Locate every Plasmodium vivax-infected red blood cell.
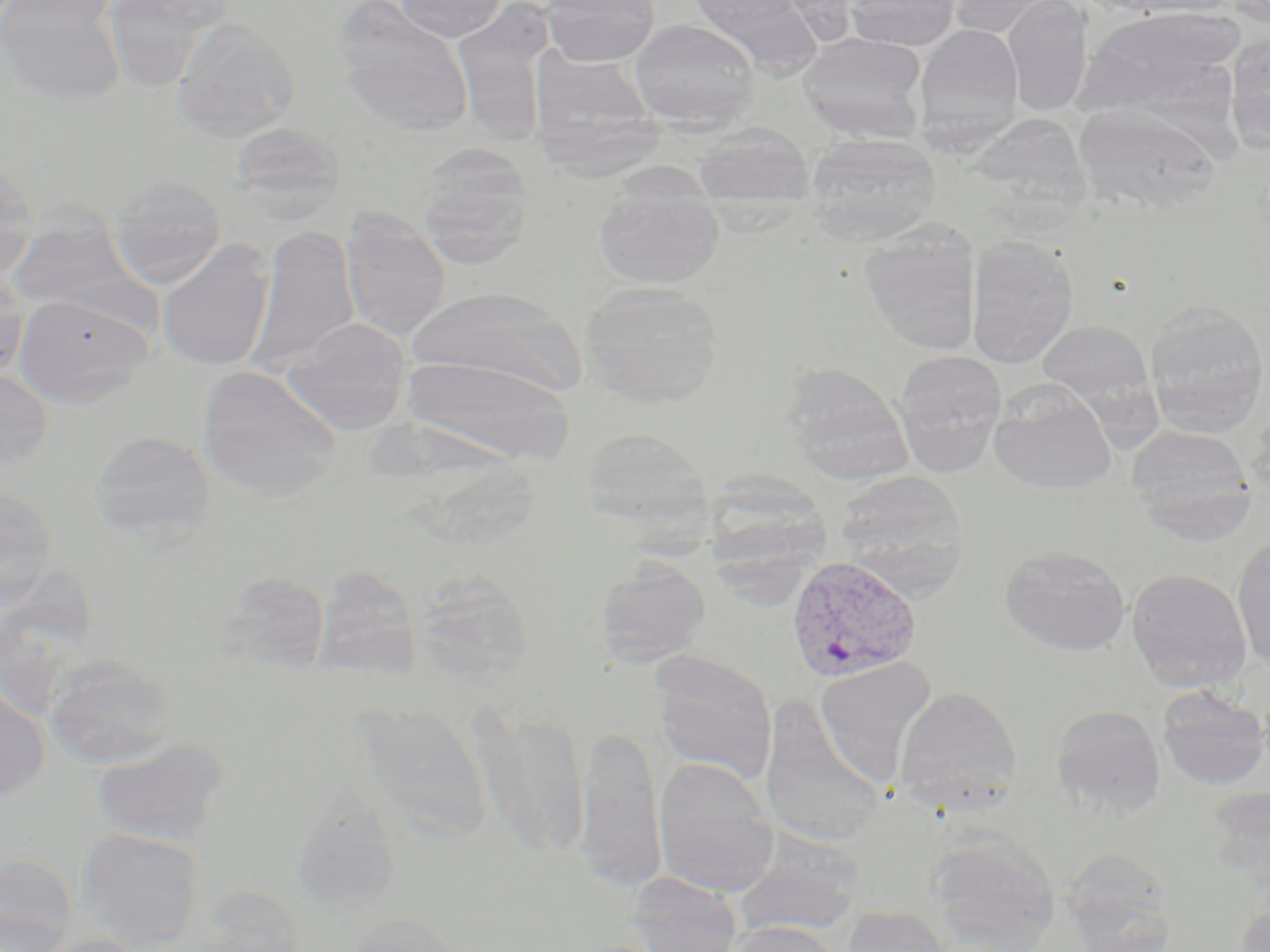
Approximate bounding boxes as [x1, y1, x2, y2] in pixels.
Plasmodium vivax-infected red blood cells: [785, 554, 923, 684].

slide-level diagnosis = Plasmodium vivax
modality = light microscopy
magnification = 1000x
field of view = single
image size = 1270×952 pixels
stain = May-Grünwald-Giemsa
preparation = thin blood film
uninfected red blood cell locations = approximate bounding boxes as [x1, y1, x2, y2] in pixels: [0, 0, 127, 105], [102, 0, 230, 92], [393, 0, 508, 41], [542, 0, 660, 66], [683, 0, 818, 65], [845, 0, 960, 51], [947, 0, 1061, 38], [1221, 0, 1270, 28], [334, 1, 474, 137], [1003, 1, 1092, 117], [458, 8, 567, 141], [1075, 9, 1244, 118], [172, 17, 300, 142], [629, 19, 760, 131], [915, 24, 1024, 146], [799, 32, 929, 143], [1224, 35, 1270, 150], [530, 45, 672, 186], [1074, 103, 1221, 214], [962, 111, 1093, 220], [230, 120, 346, 223], [693, 124, 815, 220], [807, 133, 940, 245], [417, 144, 534, 267], [0, 159, 40, 284], [594, 171, 725, 290], [109, 173, 227, 288], [340, 208, 451, 343], [6, 220, 152, 328], [859, 221, 981, 355], [249, 226, 360, 376], [965, 235, 1079, 369], [157, 240, 275, 372], [0, 272, 29, 381], [580, 281, 724, 406], [409, 285, 585, 397], [13, 293, 154, 407], [1144, 301, 1269, 436], [282, 317, 413, 434], [1036, 320, 1155, 407], [893, 350, 1007, 470], [404, 354, 575, 463], [780, 362, 911, 481], [197, 365, 340, 499], [0, 367, 54, 470], [989, 384, 1118, 495], [1245, 408, 1270, 510], [1126, 424, 1256, 539], [578, 426, 714, 534], [90, 430, 215, 545], [710, 462, 833, 608], [833, 470, 970, 588], [0, 485, 58, 606], [1231, 533, 1270, 671], [999, 545, 1131, 657], [595, 557, 711, 666], [313, 564, 422, 682], [1126, 567, 1252, 693], [410, 568, 534, 685], [216, 571, 334, 672], [650, 652, 777, 782], [43, 653, 178, 770], [813, 657, 936, 781], [0, 681, 51, 802], [894, 685, 1021, 811], [1156, 686, 1270, 791], [760, 698, 887, 848], [355, 702, 493, 840], [1051, 704, 1166, 816], [471, 705, 591, 860], [574, 726, 668, 893], [91, 738, 229, 847], [652, 756, 780, 896], [1203, 785, 1270, 888], [302, 791, 408, 900], [75, 827, 205, 949], [927, 832, 1061, 951], [734, 843, 864, 936], [1058, 847, 1178, 952], [0, 855, 77, 952], [628, 873, 743, 952], [1235, 901, 1270, 952], [841, 904, 949, 952], [336, 914, 474, 952], [725, 920, 841, 952], [33, 934, 153, 952]